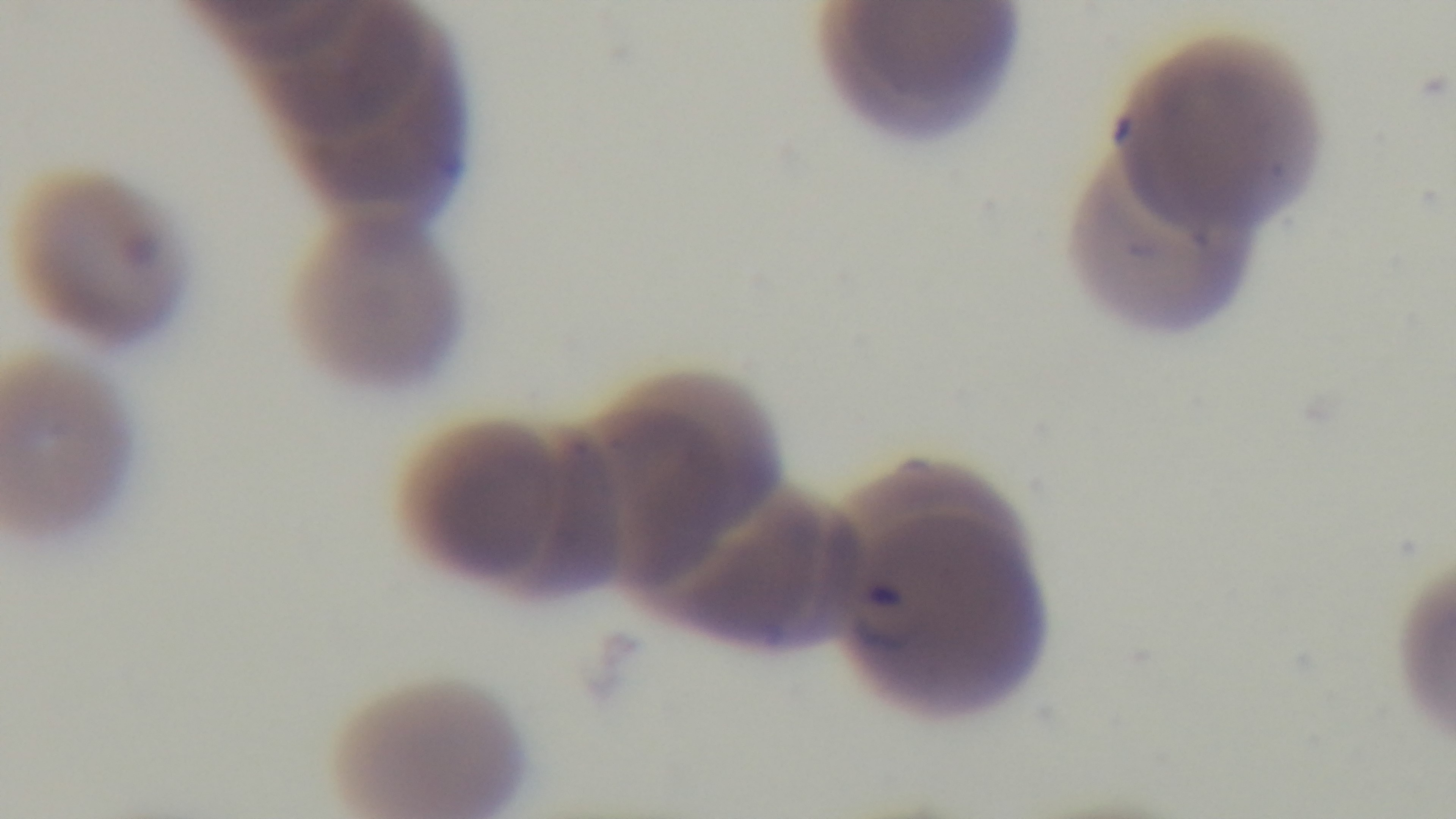
capture = mounted 4K digital camera
modality = light microscopy
field of view = single
preparation = thin
objective = 100x oil immersion
stain = Giemsa
malaria status = infected